Locate every blood parasite and identify its species.
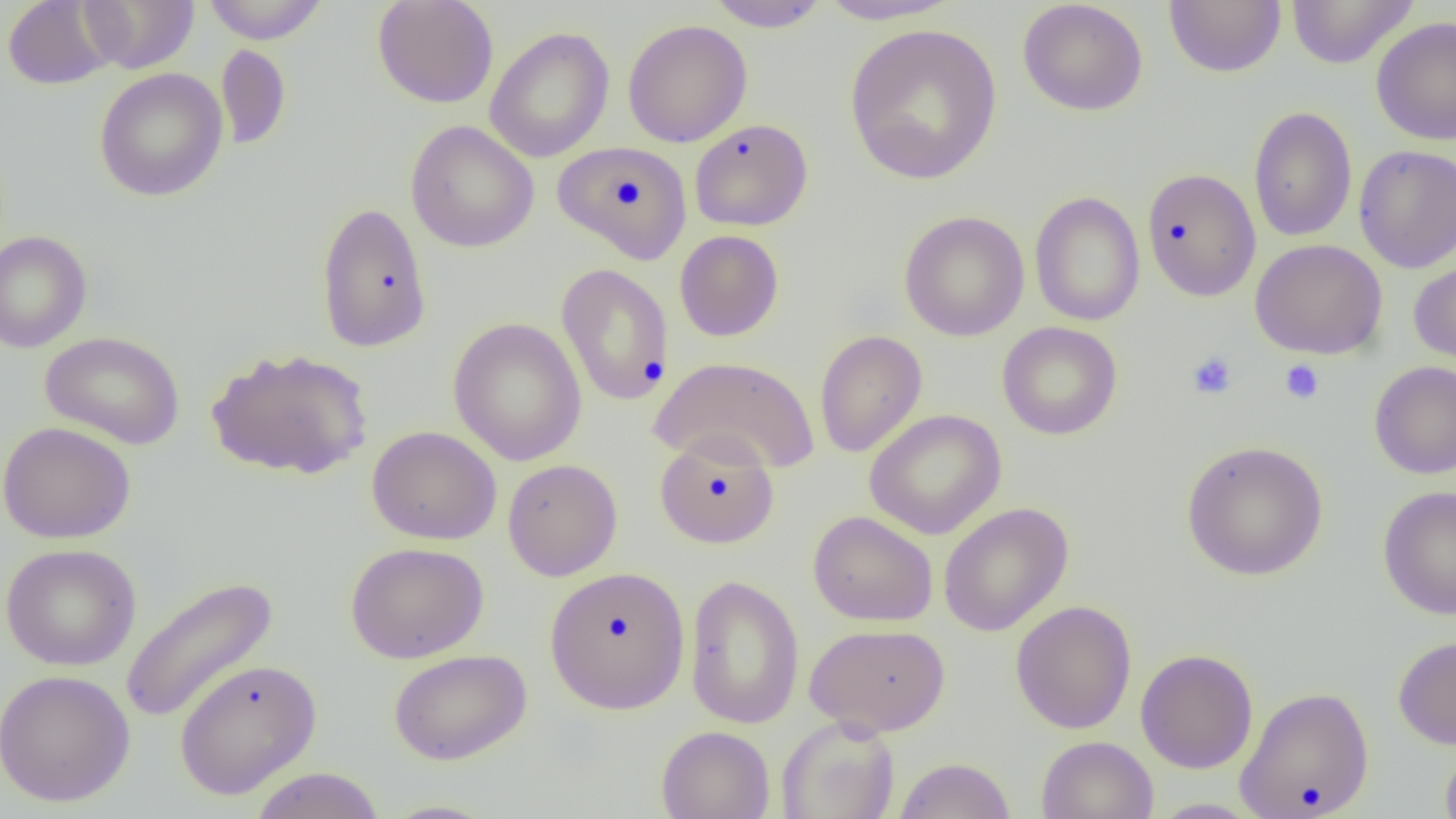
No blood parasites observed.

{
  "slide_level_diagnosis": "no evidence of blood parasites",
  "uninfected_red_blood_cell_locations": "approximate bounding boxes as (x1,y1)-(x2,y2) corner pairs in pixels: (2,0)-(118,90), (80,0)-(198,73), (201,0)-(331,44), (372,0)-(499,109), (704,0)-(830,32), (815,0)-(964,26), (1017,0)-(1149,116), (1164,0)-(1286,78), (1286,0)-(1418,69), (1370,15)-(1456,145), (623,19)-(752,148), (844,23)-(1003,185), (485,26)-(614,163), (215,44)-(291,149), (94,67)-(229,202), (1248,106)-(1358,243), (689,119)-(812,231), (405,120)-(539,253), (553,141)-(693,264), (1354,144)-(1456,272), (1142,168)-(1262,301), (1030,191)-(1145,326), (315,202)-(432,352), (899,210)-(1030,341), (0,230)-(92,353), (674,230)-(784,341), (1250,238)-(1387,359), (1408,254)-(1456,370), (556,263)-(674,406), (448,317)-(587,466), (997,321)-(1123,440), (814,330)-(927,458), (40,331)-(185,449), (205,347)-(373,481), (650,355)-(821,474), (1369,360)-(1456,479), (865,409)-(1007,539), (0,421)-(136,544), (367,425)-(502,545), (654,433)-(780,549), (1181,440)-(1328,581), (502,459)-(623,581), (1377,486)-(1456,620), (938,502)-(1073,637), (808,510)-(938,626), (345,541)-(489,664), (0,543)-(141,671), (544,566)-(690,714), (684,573)-(804,730), (119,575)-(280,724), (1009,600)-(1138,733), (804,622)-(950,737), (1393,635)-(1456,749), (388,648)-(532,766), (1135,649)-(1259,773), (174,658)-(322,800), (0,669)-(136,806), (1235,686)-(1375,819), (776,714)-(900,819), (656,725)-(775,819), (1036,735)-(1158,819), (1439,740)-(1456,819), (893,757)-(1016,818), (248,767)-(385,819), (1147,798)-(1266,818), (377,799)-(502,818)",
  "modality": "optical microscopy",
  "image_size": "1456×819 pixels",
  "field_of_view": "single",
  "preparation": "thin blood smear",
  "magnification": "1000x",
  "platelet_locations": "approximate bounding boxes as (x1,y1)-(x2,y2) corner pairs in pixels: (1187,351)-(1238,399), (1279,359)-(1325,404)"
}